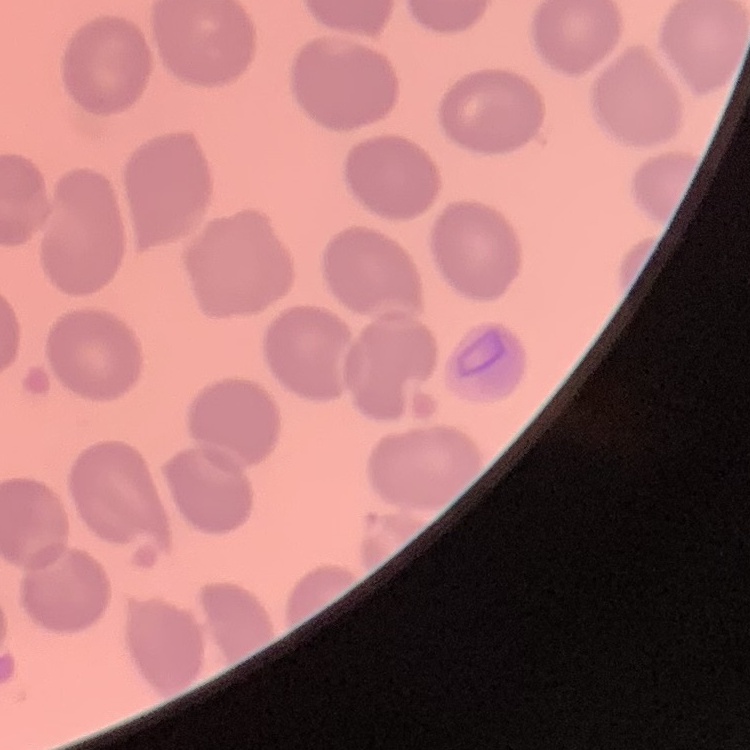

Summary:
  - Red blood cell morphology: no rouleaux formation
  - Stain: Field's or Giemsa
  - Image type: one tile cut from a larger photomicrograph
  - Preparation: thin peripheral smear